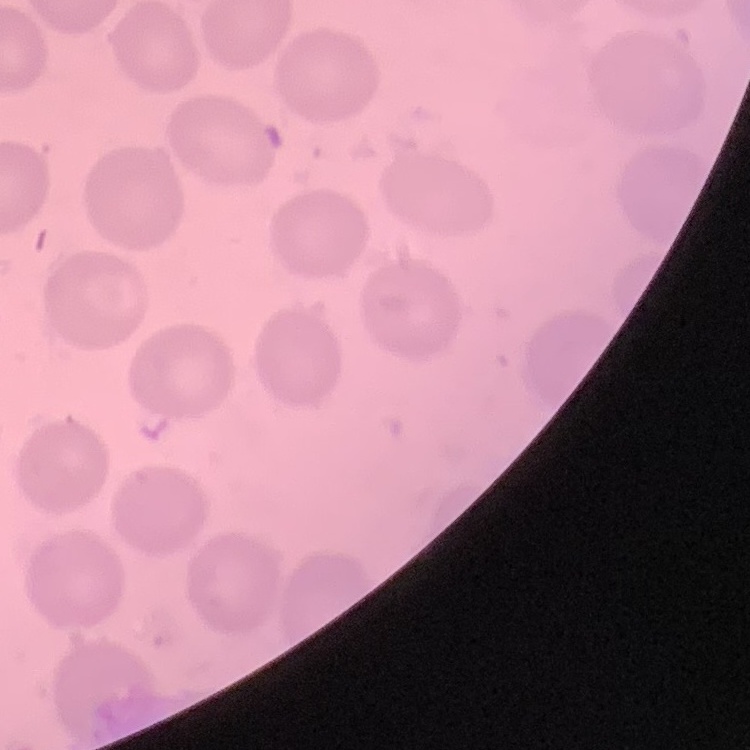
red blood cell morphology = no rouleaux formation
stain = Field's or Giemsa
image type = square crop of a larger photomicrograph
preparation = thin peripheral smear